Outline every artifact (platelet-like body, stain precipitate, or debris).
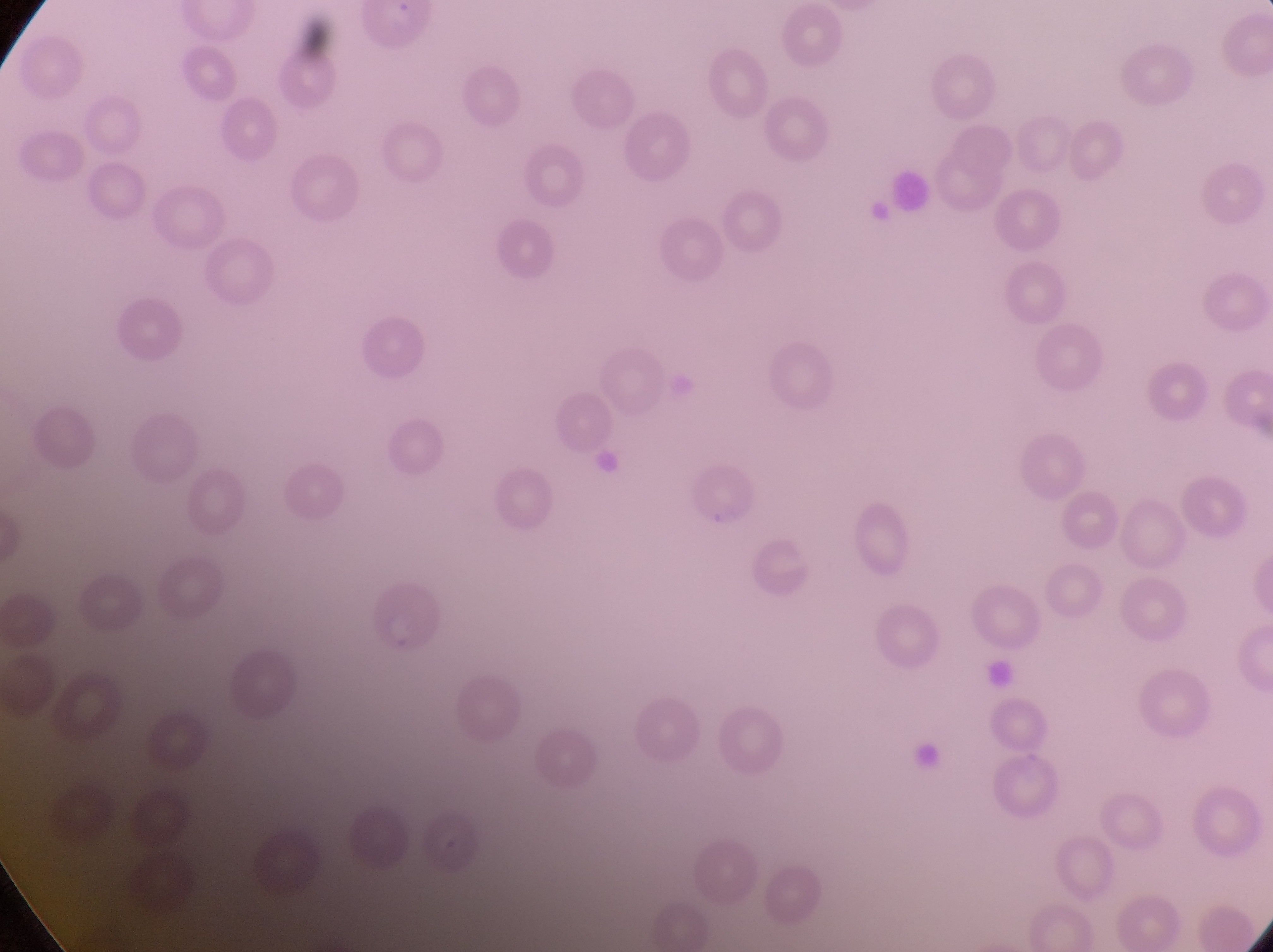
Approximate bounding boxes as {left, top, right, bottom} in pixels.
Artifacts (platelet-like body, stain precipitate, or debris): {866, 197, 898, 234}, {596, 442, 626, 479}, {903, 739, 953, 779}.

Summary:
  - Parasitised red blood cell locations: {684, 465, 758, 530}, {372, 584, 447, 656}, {424, 809, 484, 876}
  - Preparation: thin blood film
  - Capture: smartphone photograph through the eyepiece of an Olympus CX-23 microscope
  - Country: Uganda
  - Image size: 1273×952 pixels
  - Field of view: single
  - Magnification: 1000x